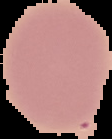
{
  "preparation": "thin blood smear",
  "image_size": "112×139 pixels",
  "result": "negative for malaria parasites",
  "image_type": "segmented cell region on a black background"
}